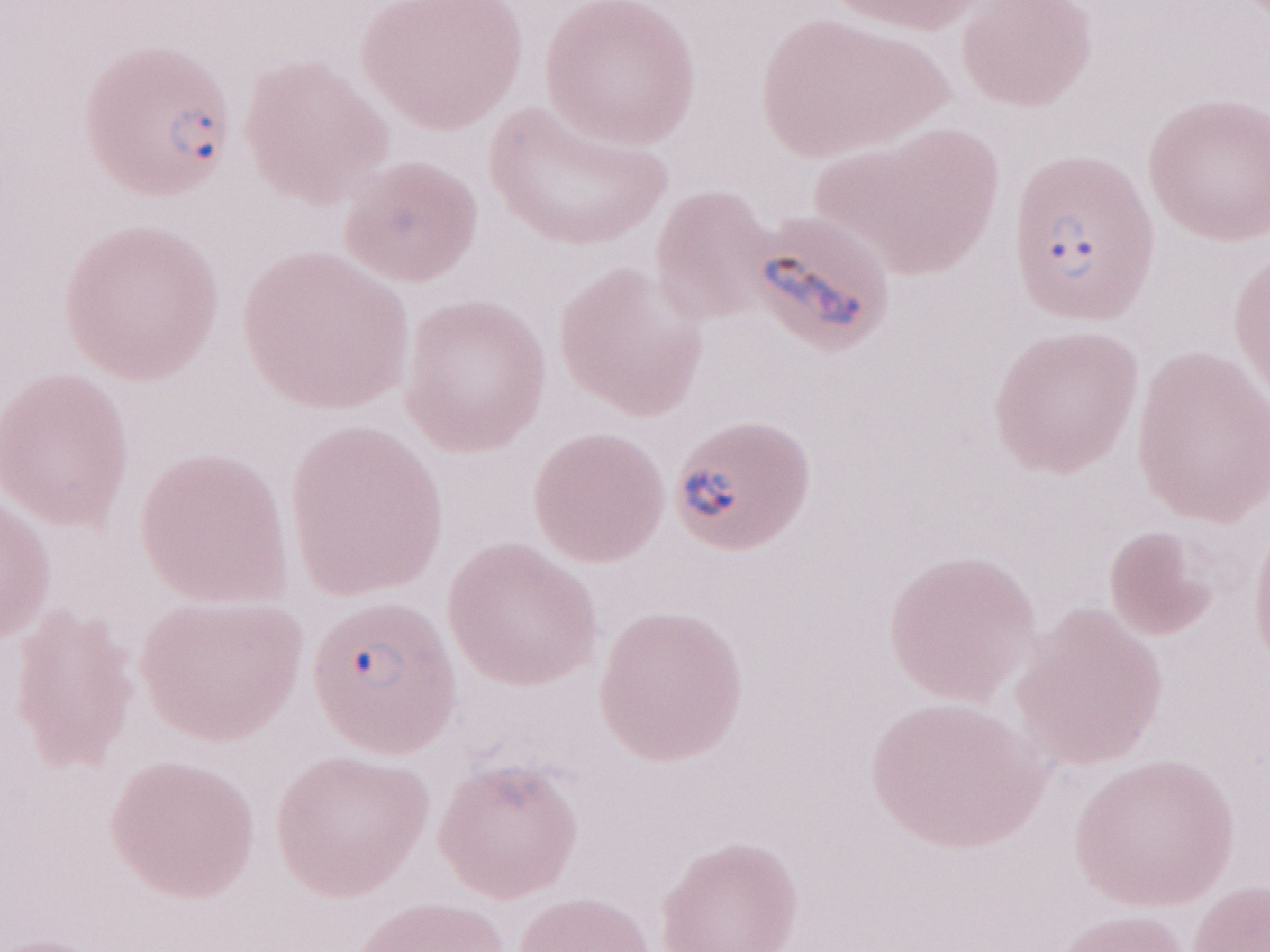 Thin peripheral-blood smear. Image is 1270×952 pixels. Magnification: 1,000x. Olympus BX43 microscope and DP73 digital camera. Single field of view. Malaria diagnosis (patient-level): positive. May-Grünwald-Giemsa stain.